Locate every malaria parasite and every leukocyte.
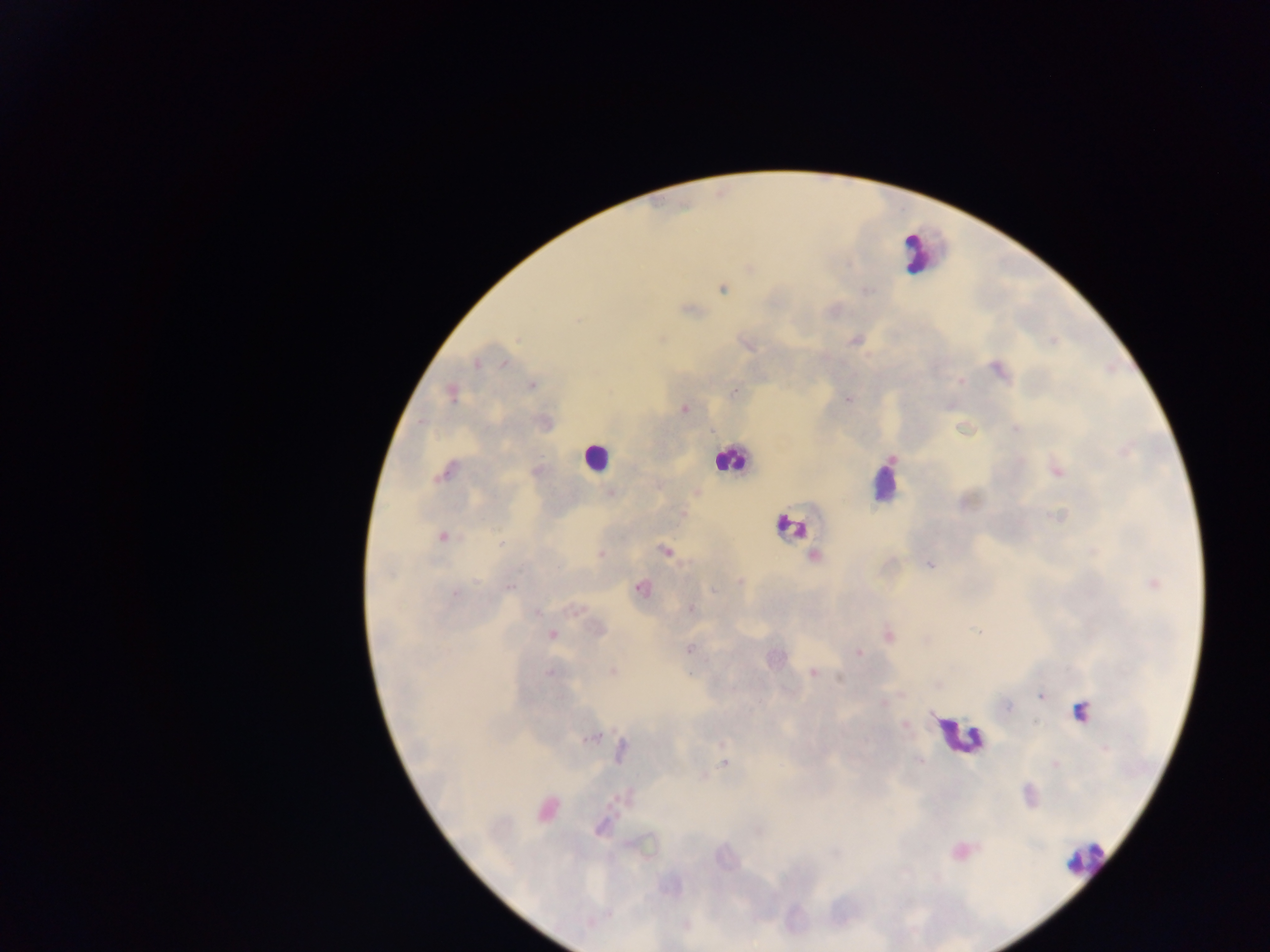
Approximate centers as (x, y) in pixels.
Malaria parasites: (722, 289), (866, 291), (688, 309), (580, 319), (517, 339), (855, 340), (1052, 340), (745, 344), (505, 364), (477, 365), (999, 370), (961, 381), (532, 386), (735, 391), (453, 394), (848, 399), (684, 409), (1015, 428), (1127, 450), (1056, 470), (537, 471), (445, 473), (611, 492), (696, 492), (683, 513), (1057, 517), (442, 536), (666, 551), (600, 554), (814, 557), (930, 564), (740, 581), (1153, 584), (510, 587), (641, 588), (713, 591), (455, 593), (690, 608), (576, 610), (535, 612), (598, 630), (978, 631), (552, 635), (889, 636), (925, 642), (690, 649), (859, 653), (549, 672), (612, 672), (813, 673), (840, 677), (936, 685), (1041, 696), (884, 704), (1007, 707), (905, 725), (592, 738), (621, 751), (919, 761), (725, 763), (1055, 764), (547, 810), (608, 914).
Leukocytes: (914, 252), (594, 457), (730, 460), (883, 480), (790, 526), (1075, 712), (958, 735), (1085, 858).

country = Ghana
field of view = single
image size = 1270×952 pixels
capture = mobile-phone photograph through a microscope
preparation = thick blood film